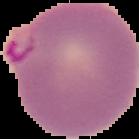
From a thin blood film. Malaria status: parasitized. The area outside the segmented cell region is set to black. Image is 139×139 pixels.